Identify the cell.
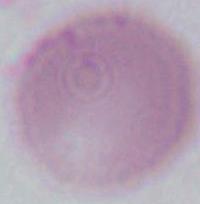
This is an erythrocyte.

Summary:
  - Magnification: 1000x
  - Modality: photomicrograph